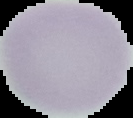
Summary:
  - Image size: 133×118 pixels
  - Preparation: thin blood smear
  - Malaria status: uninfected
  - Image type: segmented cell region with the area outside set to black